Classify this cell by malaria status.
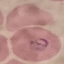
It is parasitized.

Photographed with a smartphone camera at the microscope eyepiece. Giemsa-stained preparation. Thin smear of blood. Automatically extracted cell patch, resized to 64 × 64 pixels.